Classify this cell by malaria status.
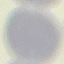

It is uninfected.

stain = Giemsa
capture = smartphone camera at the microscope eyepiece
image type = cell patch, automatically extracted from a larger field of view and resized to 64 × 64 pixels
preparation = thin blood smear